State the blood parasite species.
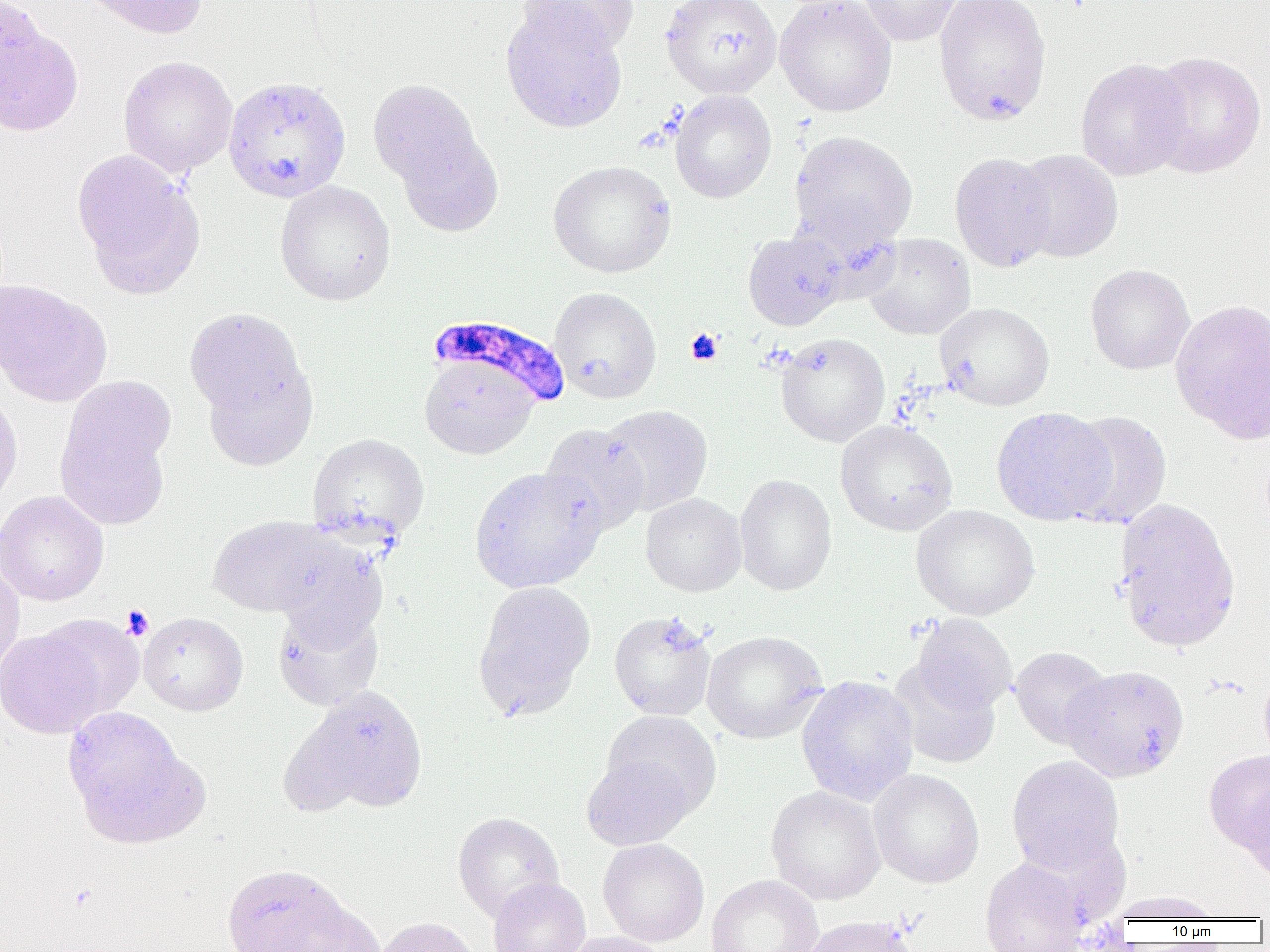
Plasmodium falciparum.

uninfected red blood cell locations = approximate bounding boxes as (x1, y1, x2, y2) in pixels: (0, 0, 47, 106), (80, 0, 208, 39), (518, 0, 637, 55), (660, 0, 782, 99), (775, 0, 897, 116), (858, 0, 965, 46), (933, 0, 1052, 125), (500, 4, 627, 133), (0, 22, 83, 136), (1147, 51, 1266, 178), (118, 56, 238, 178), (1075, 58, 1193, 181), (222, 75, 352, 203), (368, 79, 484, 191), (670, 90, 776, 203), (395, 130, 503, 237), (789, 130, 918, 249), (72, 150, 203, 295), (1012, 150, 1123, 263), (949, 152, 1057, 272), (547, 159, 677, 278), (274, 180, 396, 306), (743, 231, 849, 330), (863, 233, 976, 340), (1085, 264, 1194, 375), (0, 279, 112, 407), (549, 287, 661, 403), (1170, 298, 1270, 443), (935, 303, 1055, 410), (184, 307, 310, 423), (775, 333, 890, 447), (418, 358, 540, 460), (201, 361, 318, 470), (0, 390, 22, 513), (56, 398, 173, 531), (599, 404, 713, 515), (990, 406, 1115, 525), (1061, 410, 1173, 529), (836, 420, 958, 536), (539, 423, 650, 535), (307, 433, 429, 543), (469, 466, 607, 593), (734, 474, 837, 596), (0, 490, 109, 606), (641, 493, 746, 596), (1113, 498, 1240, 651), (911, 504, 1040, 620), (209, 515, 341, 618), (270, 538, 389, 648), (0, 556, 25, 683), (472, 581, 596, 719), (272, 605, 384, 711), (608, 610, 717, 721), (139, 612, 248, 716), (34, 613, 144, 720), (910, 614, 1016, 714), (0, 626, 107, 738), (702, 630, 827, 744), (1010, 646, 1112, 749), (889, 661, 1001, 769), (1061, 664, 1190, 783), (1258, 666, 1270, 767), (796, 676, 919, 805), (289, 686, 430, 814), (63, 705, 200, 844), (601, 711, 722, 819), (1204, 750, 1270, 855), (580, 753, 694, 851), (1006, 754, 1125, 875), (868, 769, 984, 888), (1242, 783, 1270, 887), (765, 785, 886, 905), (453, 812, 565, 922), (598, 839, 710, 946), (979, 858, 1089, 952), (221, 863, 357, 951), (706, 874, 824, 952), (487, 877, 591, 952), (1107, 890, 1225, 922), (282, 901, 389, 952), (801, 915, 920, 952), (374, 917, 480, 952), (559, 931, 673, 952)
platelet locations = approximate bounding boxes as (x1, y1, x2, y2) in pixels: (685, 328, 723, 365), (120, 604, 154, 640)
field of view = one of a larger specimen
modality = optical microscopy
image size = 1270×952 pixels
preparation = thin blood film
Plasmodium falciparum-infected red blood cell locations = approximate bounding boxes as (x1, y1, x2, y2) in pixels: (427, 314, 570, 412)
magnification = 1000x